Identify the blood parasite species.
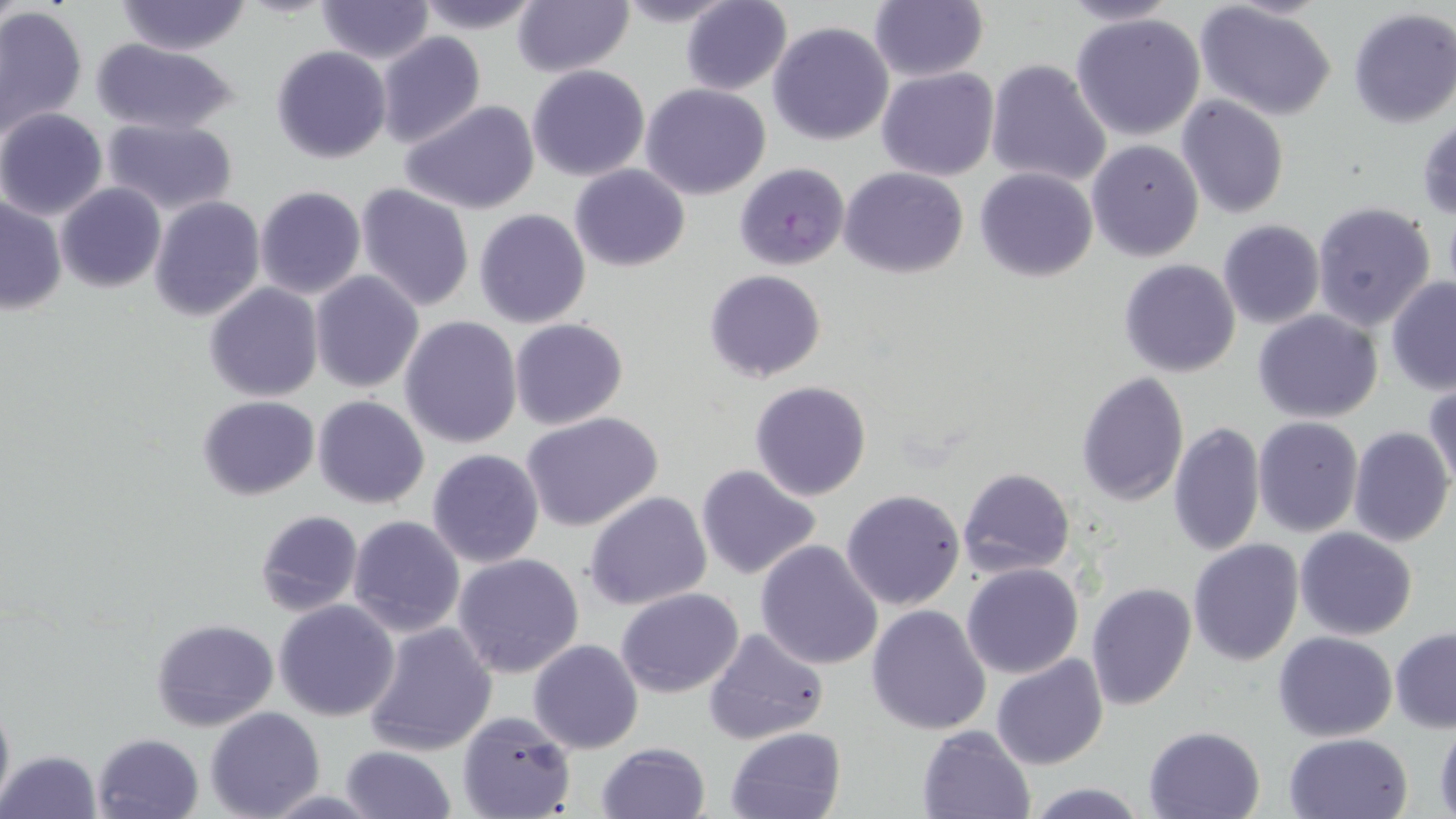
Plasmodium falciparum.

uninfected red blood cell locations = approximate bounding boxes as (x1,y1)-(x2,y2) corner pairs in pixels: (412,0)-(544,34), (511,0)-(634,77), (611,0)-(740,27), (1058,0)-(1183,27), (1195,0)-(1337,119), (113,1)-(252,54), (315,1)-(434,64), (679,1)-(792,94), (868,2)-(988,83), (0,5)-(88,136), (1347,8)-(1456,128), (1070,13)-(1207,140), (768,22)-(894,146), (376,32)-(487,148), (90,41)-(238,136), (272,45)-(391,163), (985,59)-(1112,190), (528,65)-(651,182), (878,67)-(999,181), (641,83)-(772,200), (1176,96)-(1289,218), (398,99)-(542,215), (0,109)-(109,220), (1417,115)-(1456,221), (102,117)-(238,215), (1086,139)-(1204,262), (570,164)-(690,271), (839,167)-(968,278), (974,169)-(1097,281), (56,183)-(165,294), (355,184)-(476,311), (254,185)-(366,300), (1,195)-(67,314), (148,196)-(266,321), (1311,201)-(1438,332), (474,208)-(591,328), (1217,220)-(1324,329), (1119,259)-(1241,377), (309,269)-(424,393), (703,269)-(827,384), (1386,275)-(1456,393), (204,282)-(323,402), (1253,308)-(1384,423), (399,316)-(523,449), (508,319)-(628,430), (1077,370)-(1188,505), (750,380)-(872,501), (1425,381)-(1456,496), (197,395)-(320,501), (312,395)-(430,510), (522,413)-(664,532), (1252,416)-(1363,539), (1167,419)-(1265,558), (1348,426)-(1454,547), (428,448)-(544,567), (696,464)-(823,583), (958,467)-(1076,579), (842,488)-(964,611), (585,491)-(712,610), (253,509)-(363,617), (348,516)-(465,638), (1295,526)-(1418,640), (1188,538)-(1303,665), (755,539)-(884,670), (452,553)-(585,678), (961,564)-(1084,679), (1085,582)-(1196,712), (616,587)-(744,697), (274,599)-(400,721), (867,604)-(993,735), (150,618)-(279,734), (362,619)-(497,755), (1391,627)-(1456,732), (703,628)-(829,748), (1274,631)-(1398,741), (528,640)-(643,754), (991,653)-(1108,770), (0,693)-(15,814), (206,706)-(325,818), (457,711)-(577,819), (1434,723)-(1456,819), (917,724)-(1037,818), (1144,724)-(1268,819), (726,727)-(846,819), (1283,732)-(1413,819), (92,733)-(204,819), (595,742)-(710,819), (338,746)-(457,819), (0,749)-(102,819), (1025,780)-(1150,818)
stain = May-Grünwald-Giemsa
preparation = thin blood film
field of view = single
image size = 1456×819 pixels
magnification = 1000x
modality = light microscopy
Plasmodium falciparum-infected red blood cell locations = approximate bounding boxes as (x1,y1)-(x2,y2) corner pairs in pixels: (734,161)-(847,271)